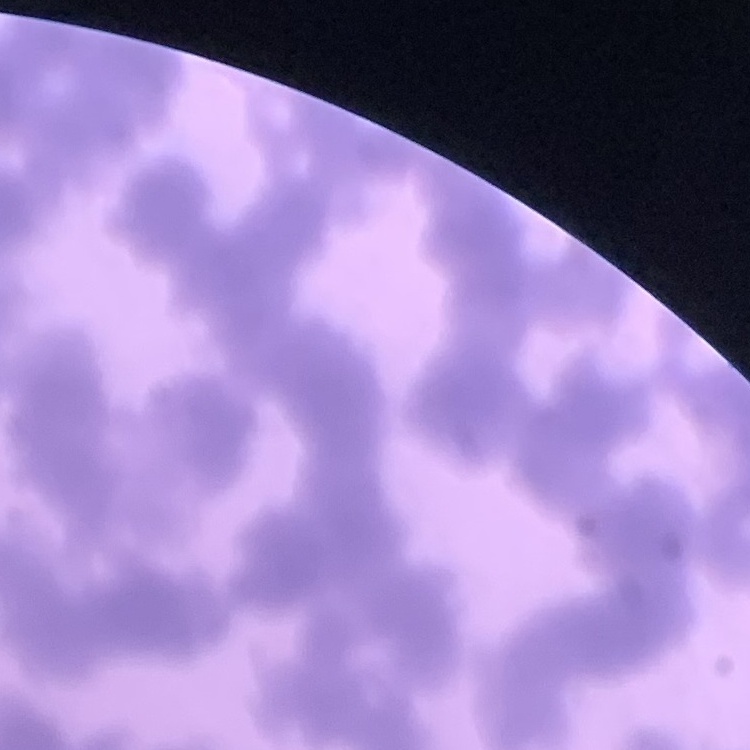

{
  "erythrocyte_morphology": "rouleaux formation",
  "preparation": "thin blood film",
  "image_type": "one tile cut from a larger photomicrograph",
  "stain": "Field's or Giemsa"
}